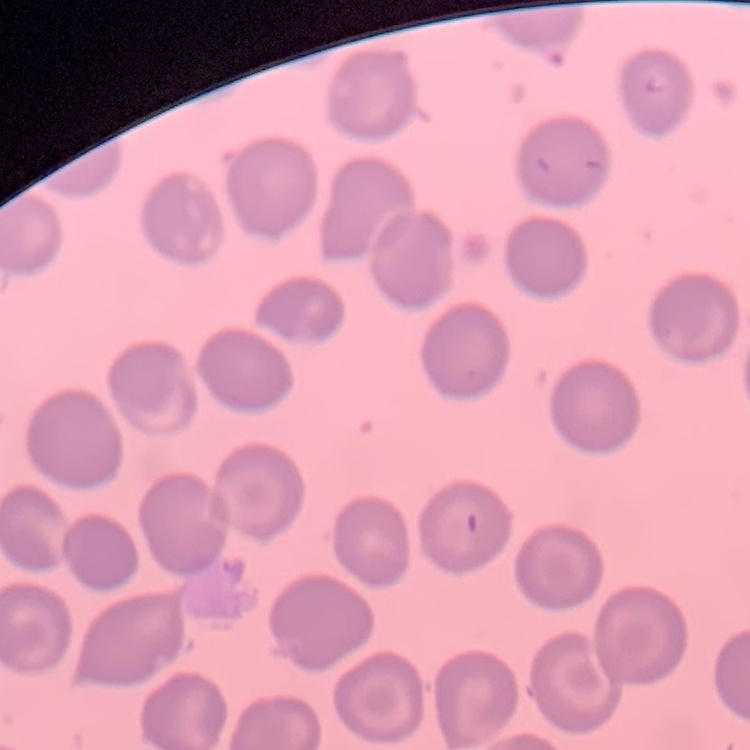
Summary:
  - Red blood cell morphology: no rouleaux formation
  - Image type: one tile cut from a larger photomicrograph
  - Stain: Field's or Giemsa
  - Preparation: thin blood film